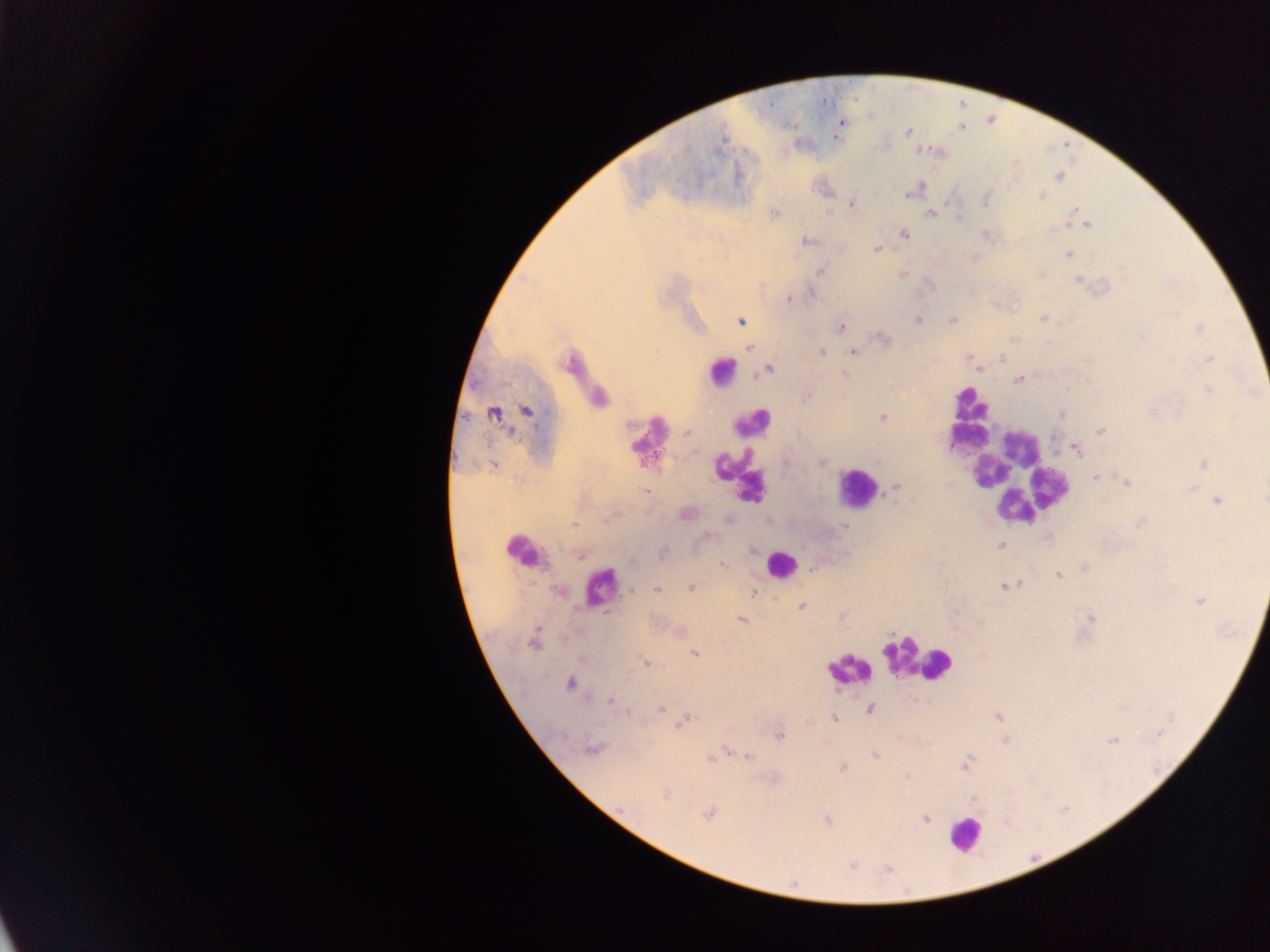 Approximate centers as {x, y} in pixels. Leukocyte locations: {574, 359}, {722, 373}, {970, 403}, {648, 436}, {968, 438}, {1019, 445}, {739, 469}, {989, 473}, {1014, 474}, {857, 488}, {520, 545}, {780, 565}, {602, 585}, {917, 661}, {848, 668}, {964, 833}. Malaria parasite locations: {841, 123}, {908, 132}, {1060, 176}, {908, 193}, {1041, 196}, {986, 200}, {853, 205}, {1075, 208}, {775, 213}, {929, 213}, {1087, 224}, {903, 234}, {808, 241}, {877, 249}, {1067, 254}, {821, 270}, {1077, 280}, {812, 294}, {788, 300}, {1044, 318}, {918, 319}, {953, 320}, {741, 321}, {841, 326}, {1199, 328}, {1142, 336}, {882, 338}, {749, 347}, {822, 352}, {853, 352}, {969, 357}, {1002, 357}, {1210, 358}, {768, 370}, {845, 374}, {1019, 380}, {1209, 390}, {808, 397}, {599, 398}, {527, 411}, {1151, 412}, {494, 413}, {1062, 414}, {883, 418}, {1101, 431}, {687, 434}, {1077, 451}, {823, 462}, {1204, 463}, {1095, 478}, {1127, 482}, {894, 489}, {647, 492}, {1217, 500}, {1264, 500}, {686, 514}, {729, 520}, {574, 525}, {845, 526}, {1001, 545}, {663, 553}, {581, 556}, {722, 564}, {1058, 574}, {1004, 586}, {690, 588}, {656, 589}, {631, 590}, {752, 593}, {1201, 601}, {802, 606}, {1091, 618}, {742, 620}, {533, 643}, {695, 653}, {645, 661}, {570, 683}, {611, 701}, {661, 708}, {871, 709}, {998, 716}, {688, 719}, {835, 719}, {1160, 735}, {780, 736}, {1113, 740}, {593, 749}, {876, 755}, {747, 756}, {711, 759}, {964, 765}, {843, 767}, {666, 794}, {973, 800}, {709, 813}, {925, 818}, {827, 821}, {852, 866}, {888, 870}. Sample from Ghana. Mobile-phone photograph taken through the microscope. Thick blood film. Single field of view. Image is 1270×952 pixels.